Assess this cell for malaria.
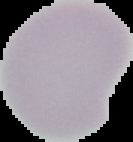
It is uninfected.

Summary:
  - Image size: 133×142 pixels
  - Preparation: thin blood film
  - Image type: cell region segmented out of the field of view; surrounding area masked to black